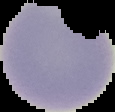

From a thin blood smear. Result: no Plasmodium parasites seen. Image is 115×112 pixels. Cell region segmented out of the field of view; the surrounding area is masked to black.